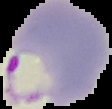
result: Plasmodium parasites detected
image_type: segmented cell region with the area outside set to black
image_size: 112×109 pixels
preparation: thin blood smear